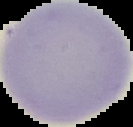

{
  "preparation": "thin blood film",
  "image_type": "segmented cell region on a black background",
  "image_size": "133×127 pixels",
  "result": "no malaria parasites seen"
}